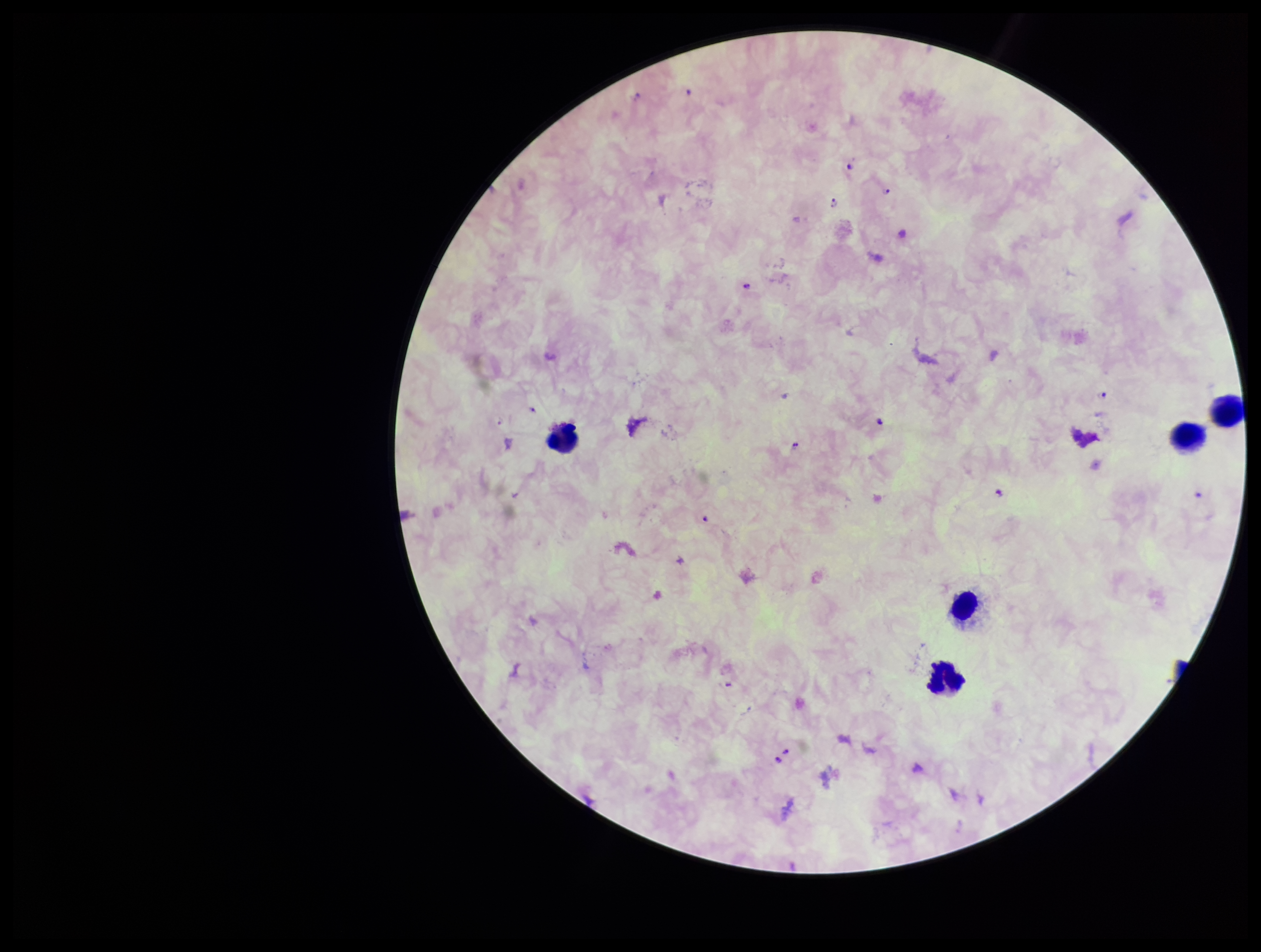
Summary:
  - Leukocyte count: 5
  - Preparation: thick
  - Patient malaria status: positive
  - Plasmodium parasites: seen
  - Capture: smartphone photograph through the microscope eyepiece
  - Field of view: single
  - Stain: Giemsa
  - Image size: 1261×952 pixels
  - Species reported for this patient: Plasmodium falciparum
  - Parasite count: 8